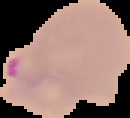 From a thin blood film. Result: Plasmodium parasites detected. Cell region segmented out of the field of view; the surrounding area is masked to black. Image is 130×118 pixels.